Mark where leukocytes are.
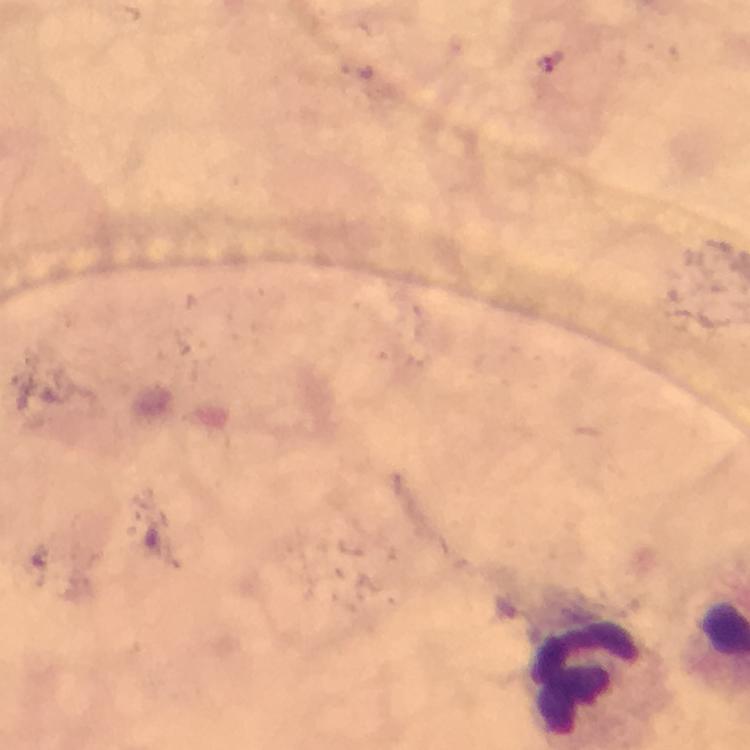
Approximate centers as (x, y) in pixels.
Leukocytes: (589, 676).

Summary:
  - Plasmodium parasites: none detected
  - Cropped from: one field of view
  - Context: from a diagnostic examination for malaria
  - Image size: 750×750 pixels
  - Immersion oil: used
  - Preparation: thick blood film
  - Capture: smartphone camera through the microscope
  - Stain: Giemsa
  - Magnification: 100x